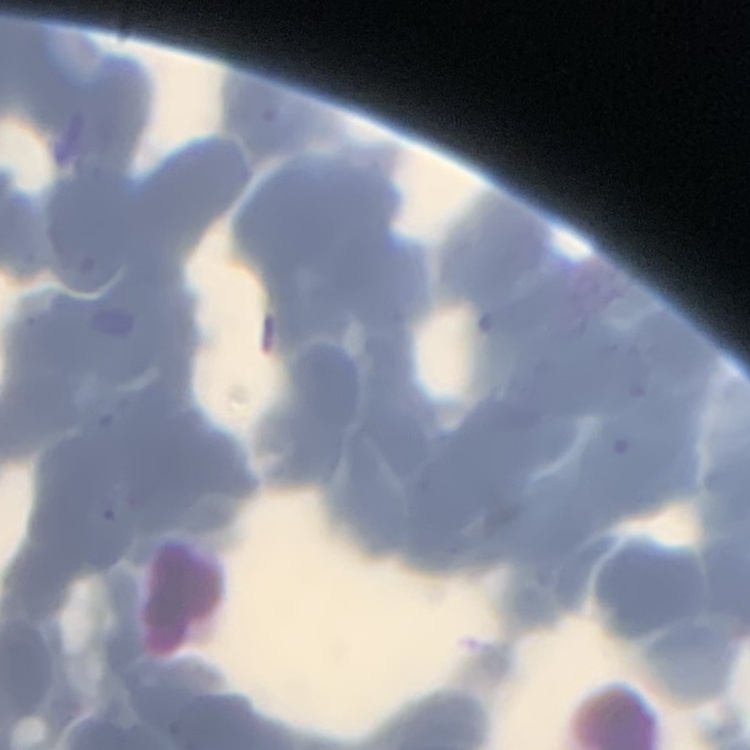

erythrocyte morphology = rouleaux formation
image type = square crop of a larger photomicrograph
stain = Field's or Giemsa
preparation = thin blood film